Classify this cell by malaria status.
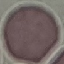

It is uninfected.

Summary:
  - Preparation: thin blood smear
  - Image type: automatically extracted cell patch, resized to 64 × 64 pixels
  - Capture: smartphone through the microscope eyepiece
  - Stain: Giemsa